Name the blood parasite species.
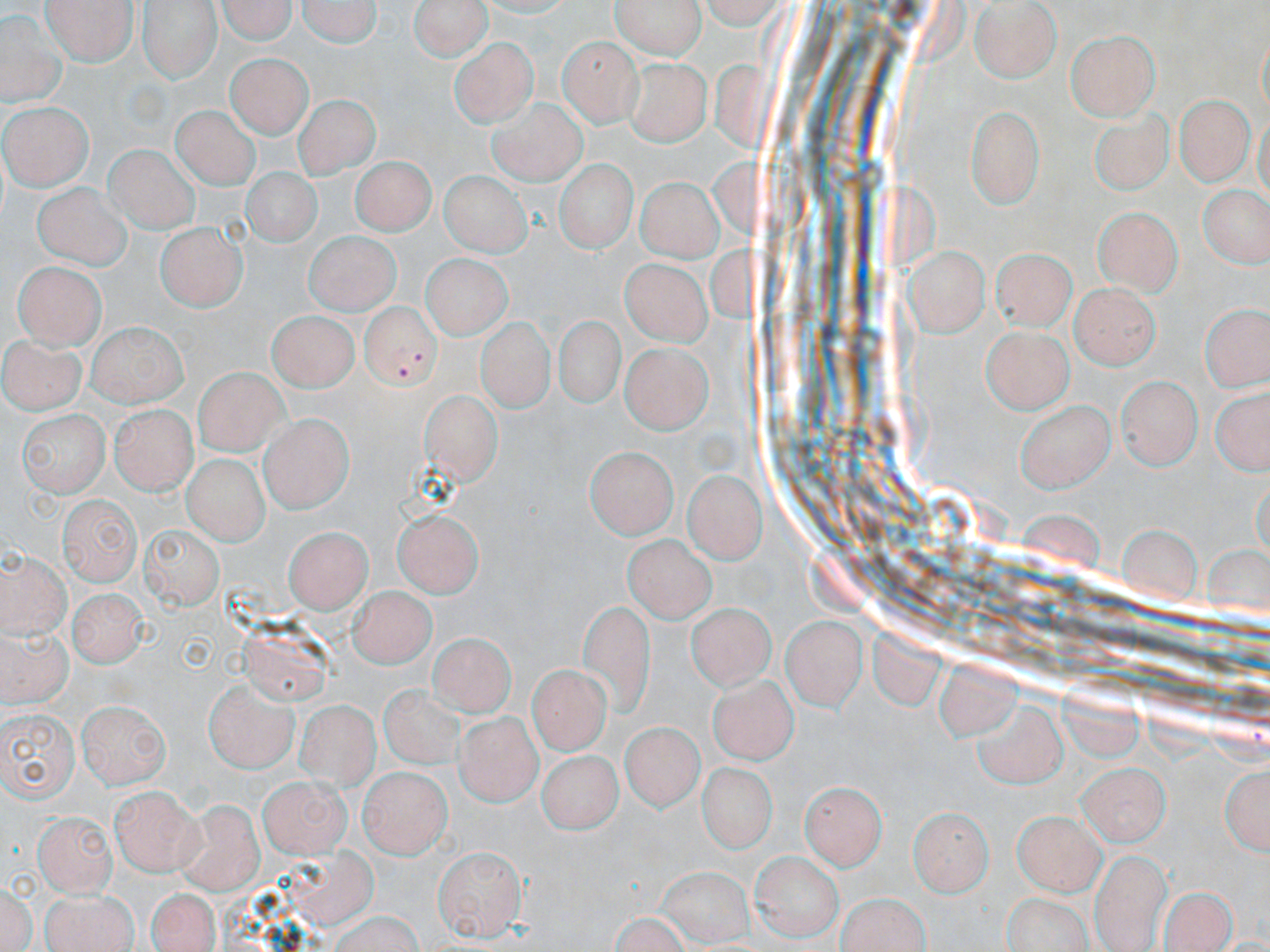
Plasmodium falciparum.

Approximate bounding boxes as [x1, y1, x2, y2] in pixels. Uninfected red blood cell locations: [40, 0, 137, 66], [136, 0, 219, 81], [213, 0, 302, 44], [296, 0, 382, 50], [610, 0, 707, 57], [412, 2, 488, 65], [969, 2, 1060, 81], [427, 9, 528, 101], [1, 13, 59, 105], [1065, 30, 1161, 118], [556, 36, 637, 123], [450, 37, 538, 125], [230, 52, 309, 134], [622, 57, 709, 148], [1176, 95, 1249, 184], [293, 97, 382, 191], [487, 98, 586, 184], [4, 101, 94, 190], [965, 104, 1045, 205], [172, 105, 260, 188], [1085, 105, 1179, 199], [106, 143, 198, 233], [352, 156, 430, 236], [553, 157, 639, 253], [242, 168, 320, 249], [438, 170, 527, 259], [636, 176, 716, 263], [33, 180, 128, 272], [1196, 183, 1270, 271], [1093, 203, 1185, 292], [157, 221, 244, 313], [300, 230, 401, 314], [987, 245, 1080, 335], [903, 247, 987, 334], [423, 255, 508, 340], [616, 259, 715, 345], [12, 261, 105, 348], [1071, 284, 1157, 367], [1199, 296, 1269, 390], [265, 310, 358, 390], [551, 313, 623, 410], [477, 317, 551, 414], [84, 320, 188, 404], [980, 325, 1071, 412], [4, 333, 83, 412], [618, 340, 708, 433], [192, 367, 288, 455], [1118, 376, 1198, 469], [1208, 387, 1270, 476], [423, 391, 500, 480], [1018, 397, 1115, 492], [18, 408, 108, 494], [105, 408, 194, 491], [259, 416, 352, 510], [583, 445, 678, 539], [179, 452, 265, 545], [682, 468, 764, 564], [57, 490, 141, 584], [394, 508, 482, 599], [138, 517, 219, 608], [1116, 519, 1205, 608], [283, 527, 371, 615], [621, 535, 721, 625], [1, 542, 75, 639], [350, 583, 433, 666], [69, 586, 151, 668], [578, 602, 656, 725], [688, 604, 775, 694], [781, 612, 869, 709], [1, 623, 79, 709], [429, 636, 513, 723], [529, 664, 607, 753], [708, 673, 797, 762], [380, 675, 471, 773], [201, 677, 297, 773], [297, 698, 377, 785], [76, 701, 172, 789], [971, 701, 1066, 789], [0, 706, 77, 803], [449, 709, 544, 806], [617, 719, 707, 816], [538, 751, 622, 835], [695, 760, 773, 858], [1076, 762, 1170, 846], [1219, 763, 1267, 857], [358, 765, 451, 855], [258, 772, 350, 854], [797, 776, 888, 869], [109, 786, 196, 875], [172, 798, 262, 895], [907, 804, 993, 895], [1013, 808, 1104, 892], [36, 811, 120, 894], [431, 842, 525, 938], [1092, 848, 1170, 951], [746, 851, 844, 942], [2, 882, 38, 951], [1160, 884, 1236, 952], [144, 889, 223, 952], [38, 890, 139, 952], [835, 893, 932, 952], [324, 912, 427, 952]. Plasmodium falciparum-infected red blood cell locations: [358, 300, 439, 390]. Thin blood film. Image is 1270×952 pixels. Captured at 1000x magnification. One field of a larger specimen. May-Grünwald-Giemsa stain. Light microscopy.